Identify the blood parasite species.
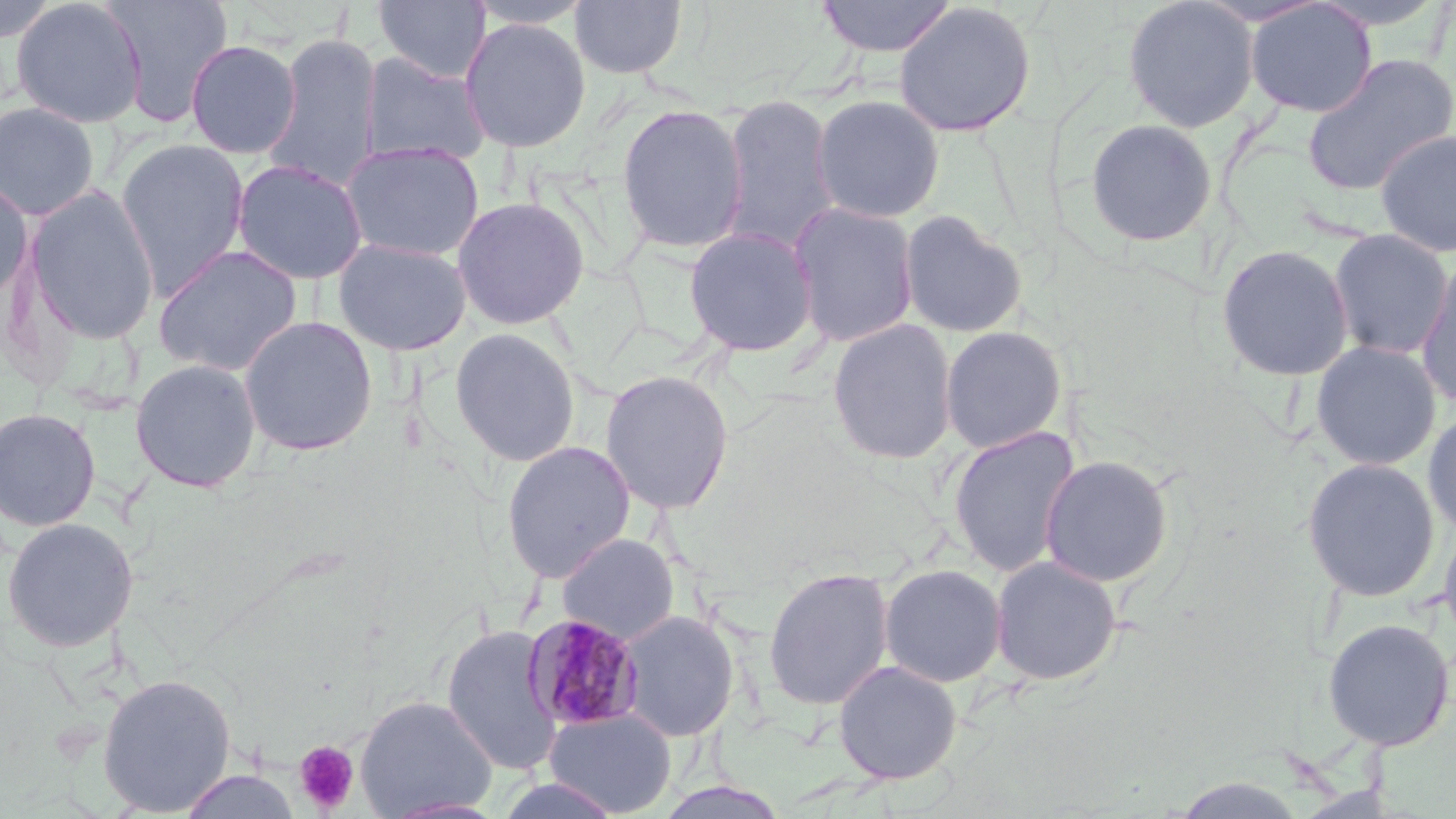

Plasmodium malariae.

Approximate bounding boxes as (x1,y1)-(x2,y2) corner pairs in pixels. Uninfected red blood cell locations: (11,0)-(147,128), (102,0)-(233,127), (373,0)-(490,83), (465,0)-(596,28), (814,0)-(958,57), (1122,0)-(1260,133), (1305,0)-(1454,32), (2,1)-(61,43), (570,1)-(687,79), (1244,1)-(1377,118), (892,2)-(1037,138), (459,18)-(591,152), (261,33)-(383,193), (185,39)-(301,159), (360,53)-(491,167), (1301,53)-(1456,197), (720,93)-(839,254), (810,95)-(946,222), (0,101)-(101,221), (616,103)-(749,254), (1084,118)-(1218,248), (1374,129)-(1456,257), (115,138)-(250,299), (341,141)-(484,263), (232,159)-(368,285), (0,177)-(33,306), (25,185)-(160,346), (452,196)-(590,329), (789,201)-(920,348), (898,210)-(1029,338), (683,226)-(819,357), (1328,229)-(1454,360), (333,238)-(472,356), (1215,243)-(1355,382), (152,244)-(304,378), (1416,254)-(1456,412), (239,316)-(378,456), (827,319)-(958,465), (940,326)-(1067,453), (449,327)-(582,467), (1311,340)-(1442,471), (129,358)-(262,493), (600,370)-(734,515), (1422,406)-(1456,541), (0,407)-(102,532), (947,426)-(1081,578), (500,441)-(636,583), (1039,455)-(1175,587), (1301,457)-(1441,602), (1439,515)-(1456,654), (1,517)-(139,652), (557,534)-(679,644), (989,555)-(1123,686), (879,563)-(1007,687), (762,566)-(895,712), (617,609)-(739,742), (1322,618)-(1454,751), (441,624)-(563,775), (833,660)-(963,785), (96,673)-(236,816), (354,695)-(498,818), (544,708)-(677,817), (179,770)-(301,818), (652,780)-(793,819). Plasmodium malariae-infected red blood cell locations: (522,614)-(646,732). Platelet locations: (294,741)-(360,814). Thin blood film. 1000x magnification. Image is 1456×819 pixels. Optical microscopy. May-Grünwald-Giemsa stain. Single field of view.